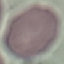
Summary:
  - Malaria status: uninfected
  - Stain: Giemsa
  - Image type: automatically extracted cell patch, resized to 64 × 64 pixels
  - Capture: smartphone through the microscope eyepiece
  - Preparation: thin blood film